Describe the morphology of the red blood cells.
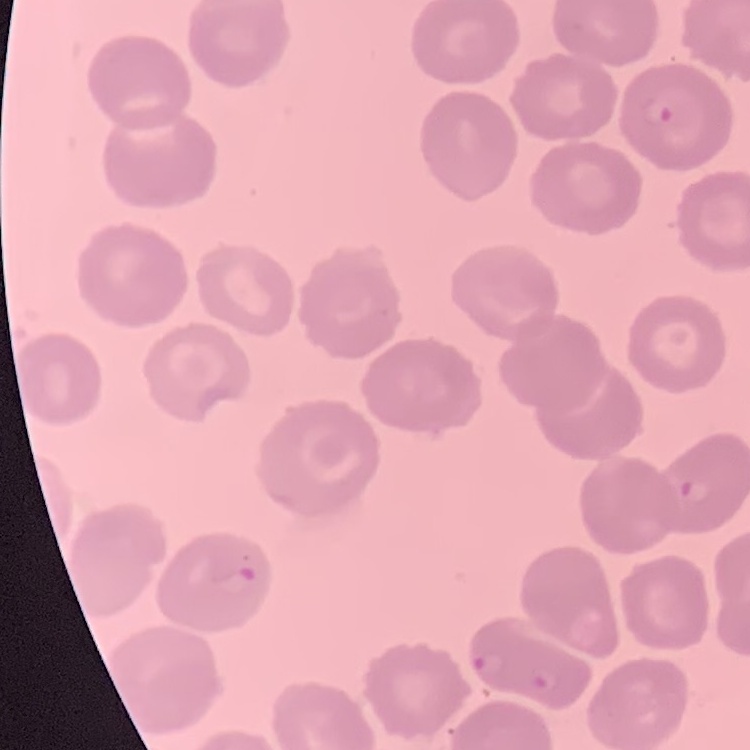
They show no rouleaux formation.

Thin blood film. Square crop of a larger photomicrograph. Field's or Giemsa stain.